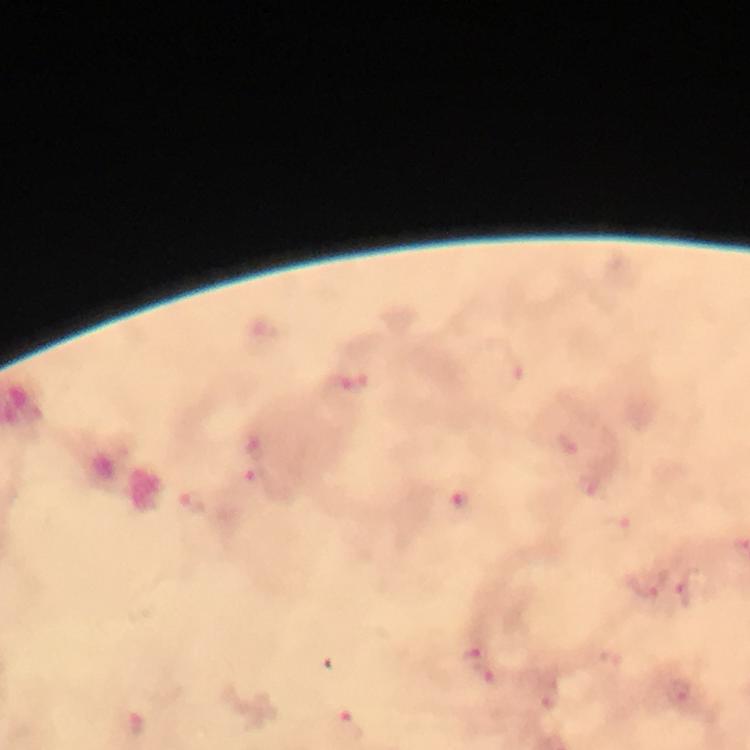
immersion_oil: used
malaria_parasite_locations: 'approximate centers as (x, y) in pixels: (341, 384), (255, 478), (590, 485), (463, 499), (193, 501), (643, 586), (687, 590)'
capture: smartphone photograph through a microscope
image_size: 750×750 pixels
preparation: thick smear
context: from a malaria diagnostic workup
cropped_from: a single field of view
magnification: 100x
stain: Giemsa